Locate every Plasmodium ovale-infected red blood cell.
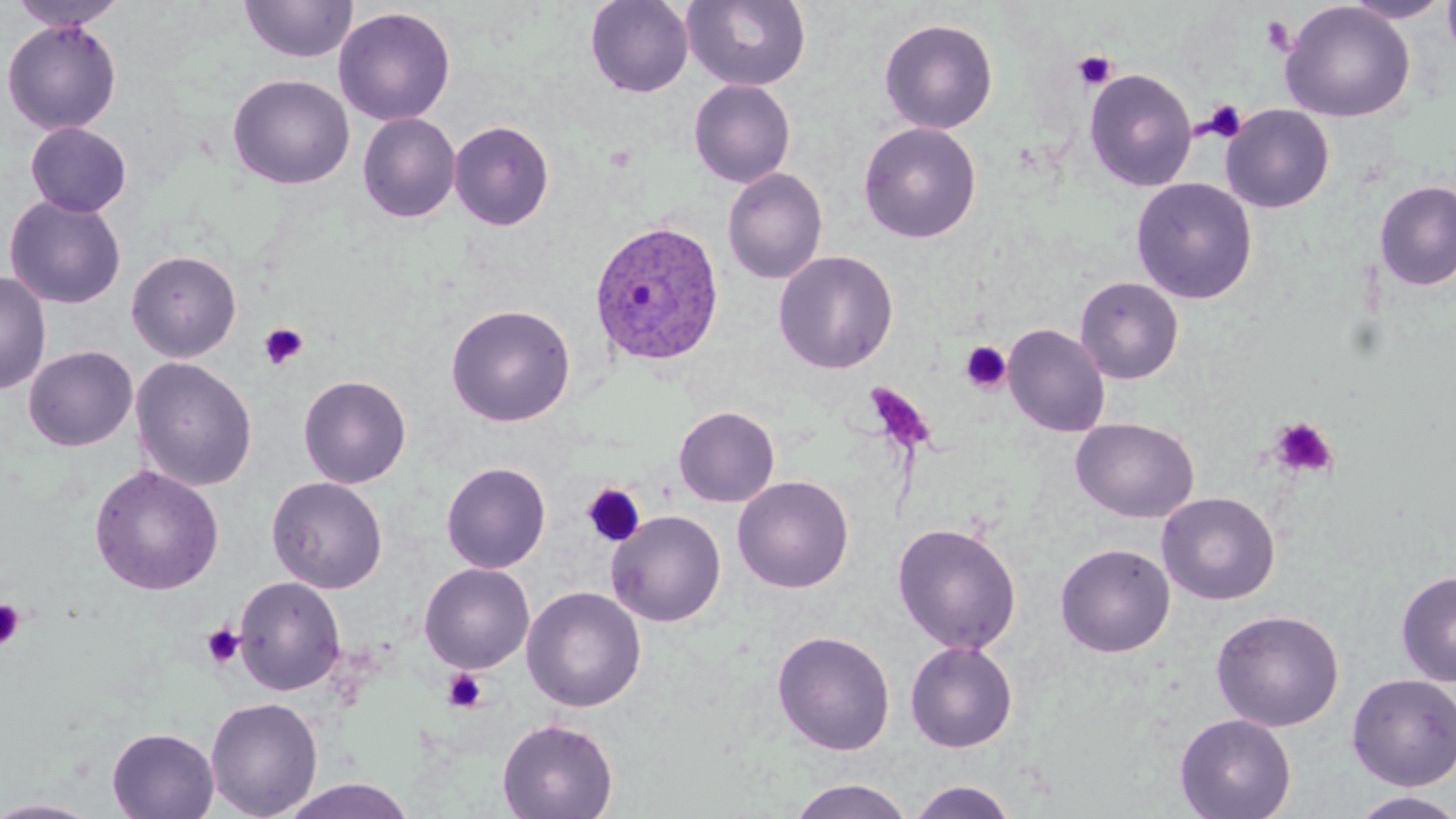

Approximate bounding boxes as (x1, y1, x2, y2) in pixels.
Plasmodium ovale-infected red blood cells: (588, 219, 726, 369).

Platelet locations: (1073, 50, 1117, 91), (1200, 99, 1247, 142), (258, 322, 309, 370), (960, 341, 1012, 394), (865, 383, 937, 455), (1269, 416, 1338, 479), (582, 483, 645, 548), (0, 598, 26, 651), (201, 623, 245, 669), (441, 668, 488, 714). Uninfected red blood cell locations: (240, 0, 358, 63), (585, 0, 694, 98), (683, 0, 811, 92), (1341, 0, 1453, 23), (1441, 0, 1456, 62), (8, 1, 130, 32), (1280, 2, 1416, 122), (333, 6, 456, 126), (1, 18, 123, 136), (879, 18, 998, 134), (1084, 68, 1198, 192), (227, 73, 355, 190), (688, 79, 796, 188), (1220, 104, 1335, 213), (358, 113, 460, 223), (449, 120, 554, 230), (24, 122, 132, 217), (859, 122, 981, 243), (722, 168, 828, 285), (1131, 177, 1258, 304), (1374, 179, 1456, 291), (4, 194, 127, 309), (126, 249, 242, 362), (773, 250, 898, 374), (0, 270, 51, 396), (1075, 276, 1184, 384), (445, 303, 576, 427), (1003, 323, 1110, 437), (23, 345, 138, 452), (131, 356, 257, 492), (298, 374, 411, 489), (674, 406, 780, 507), (1071, 417, 1199, 523), (441, 461, 551, 573), (89, 463, 224, 596), (733, 475, 853, 593), (267, 476, 388, 593), (1157, 491, 1280, 605), (607, 510, 726, 627), (893, 522, 1022, 654), (1055, 542, 1176, 657), (419, 563, 535, 673), (1396, 570, 1456, 687), (233, 575, 346, 695), (522, 586, 647, 712), (1210, 608, 1345, 732), (772, 629, 895, 755), (905, 640, 1018, 752), (1346, 673, 1456, 790), (206, 697, 323, 818), (1175, 713, 1296, 819), (497, 718, 618, 819), (107, 726, 220, 819), (278, 777, 418, 819), (786, 778, 913, 819), (906, 780, 1020, 819), (1348, 791, 1456, 819), (0, 798, 106, 818). Slide-level diagnosis: Plasmodium ovale. May-Grünwald-Giemsa stain. Thin blood smear. Optical microscopy. One field of a larger specimen. Captured at 1000x magnification. Image is 1456×819 pixels.